Identify the cell.
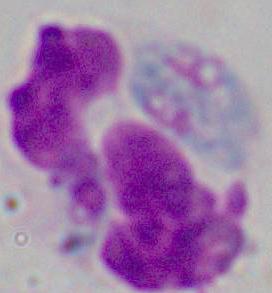
This is a leukocyte.

1000x magnification. Micrograph.